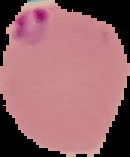
Summary:
  - Result: Plasmodium parasites identified
  - Image type: cell region segmented out of the field of view; surrounding area masked to black
  - Image size: 130×157 pixels
  - Preparation: thin blood smear